Identify the preparation type.
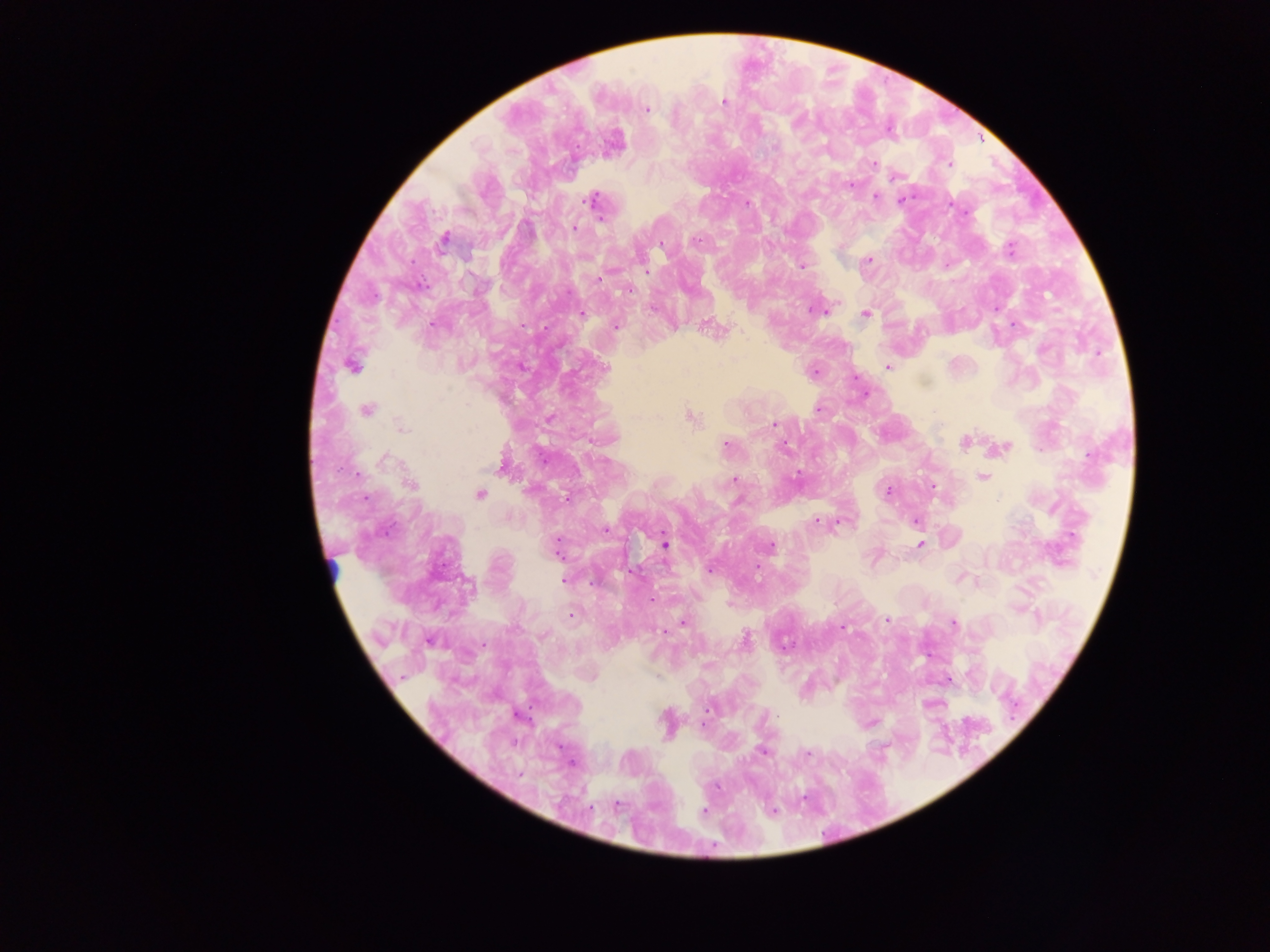

Thick blood smear.

Approximate centers as (x, y) in pixels. Leukocyte locations: (334, 571). Malaria parasite locations: (725, 102), (646, 109), (613, 145), (873, 163), (950, 163), (895, 176), (850, 185), (875, 196), (592, 200), (901, 200), (747, 203), (573, 227), (444, 239), (696, 241), (661, 244), (1009, 248), (867, 260), (801, 266), (646, 273), (628, 289), (818, 308), (996, 308), (581, 314), (865, 314), (616, 326), (708, 327), (351, 365), (888, 367), (605, 369), (813, 371), (818, 408), (367, 409), (690, 417), (773, 424), (401, 428), (964, 440), (725, 445), (784, 446), (1000, 448), (503, 463), (982, 477), (734, 481), (411, 484), (932, 487), (888, 490), (480, 494), (567, 498), (815, 520), (916, 521), (839, 522), (605, 530), (920, 544), (664, 545), (769, 546), (556, 548), (756, 567), (710, 568), (564, 580), (652, 599), (571, 613), (887, 620), (682, 622), (953, 622), (843, 628), (744, 640), (947, 680), (518, 715), (666, 722), (870, 722), (701, 725), (763, 752), (806, 754), (571, 763), (704, 811), (772, 812). Image is 1270×952 pixels. Single field of view. Sample from Ghana. Photographed through a microscope with a mobile-phone camera.